Name the parasite shown.
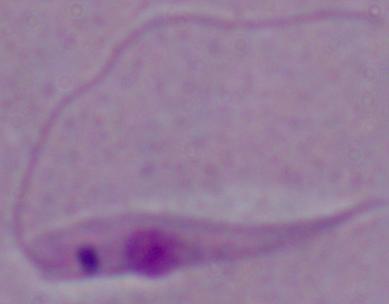
This is Leishmania.

magnification: 1000x
modality: photomicrograph